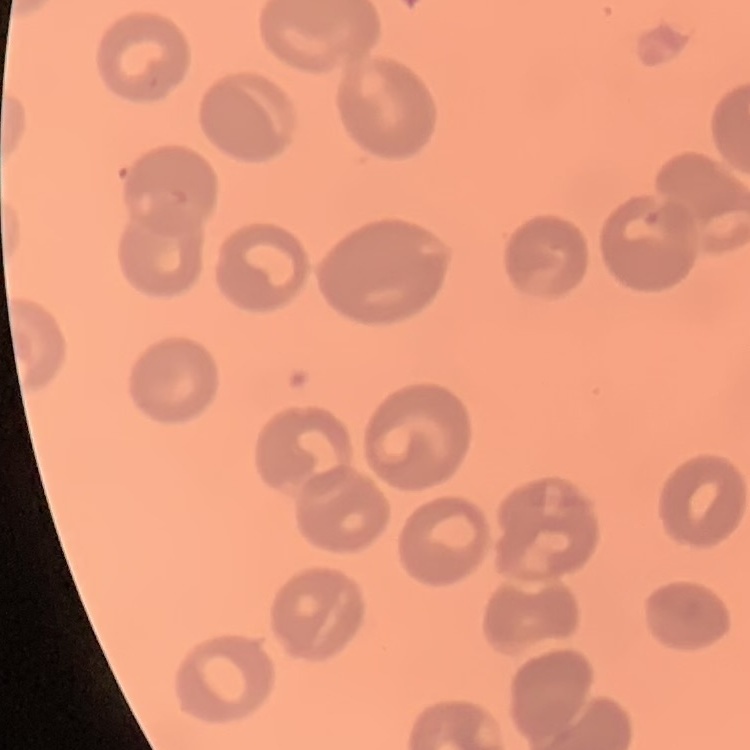
{
  "erythrocyte_morphology": "no rouleaux formation",
  "stain": "Field's or Giemsa",
  "preparation": "thin peripheral smear",
  "image_type": "square crop of a larger photomicrograph"
}